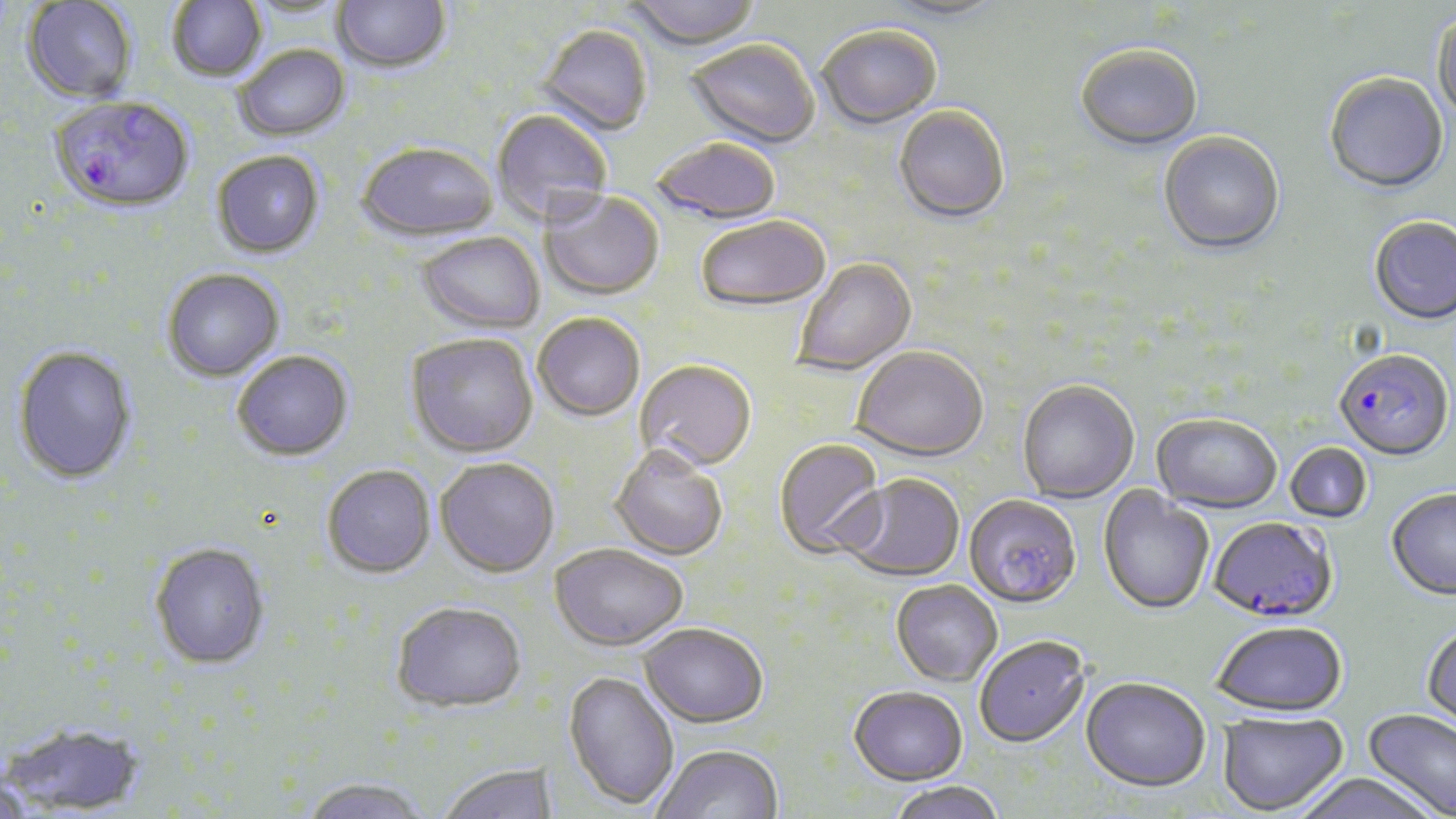
Approximate bounding boxes as (x1, y1, x2, y2) in pixels. Plasmodium falciparum-infected red blood cell locations: (50, 99, 194, 217), (1334, 351, 1453, 464), (1209, 519, 1338, 626). Uninfected red blood cell locations: (167, 0, 267, 84), (332, 0, 451, 76), (625, 0, 761, 53), (22, 1, 137, 106), (241, 1, 352, 21), (876, 1, 1009, 25), (1431, 13, 1456, 124), (535, 26, 653, 138), (818, 28, 942, 131), (685, 41, 819, 150), (234, 46, 351, 144), (1075, 47, 1203, 153), (1323, 74, 1449, 196), (893, 107, 1009, 226), (492, 111, 612, 229), (1158, 133, 1285, 257), (652, 139, 782, 226), (357, 145, 499, 244), (212, 152, 324, 261), (539, 192, 664, 303), (695, 217, 831, 316), (1369, 218, 1456, 327), (416, 233, 545, 336), (792, 259, 918, 377), (163, 270, 284, 383), (533, 315, 645, 423), (405, 335, 539, 461), (11, 347, 138, 485), (851, 348, 989, 464), (232, 352, 354, 464), (635, 362, 757, 475), (1017, 381, 1139, 504), (1151, 415, 1281, 516), (774, 440, 887, 561), (1284, 443, 1373, 525), (610, 449, 727, 562), (435, 460, 559, 580), (322, 467, 436, 581), (839, 475, 965, 584), (1097, 487, 1214, 617), (1386, 491, 1456, 603), (964, 496, 1081, 611), (150, 545, 271, 673), (549, 546, 687, 654), (891, 582, 1002, 688), (391, 605, 528, 716), (1212, 624, 1348, 720), (638, 626, 768, 730), (1422, 626, 1456, 735), (974, 638, 1091, 750), (563, 672, 679, 812), (1080, 679, 1210, 796), (848, 689, 968, 789), (1362, 709, 1456, 819), (1217, 713, 1349, 817), (4, 722, 147, 816), (653, 746, 784, 819), (439, 765, 559, 819), (1294, 776, 1441, 818), (0, 777, 36, 819), (299, 780, 429, 819), (889, 782, 1006, 819). Slide-level diagnosis: Plasmodium falciparum. Single field of view. 1000x magnification. Thin blood film. May-Grünwald-Giemsa-stained preparation. Image is 1456×819 pixels. Light microscopy.